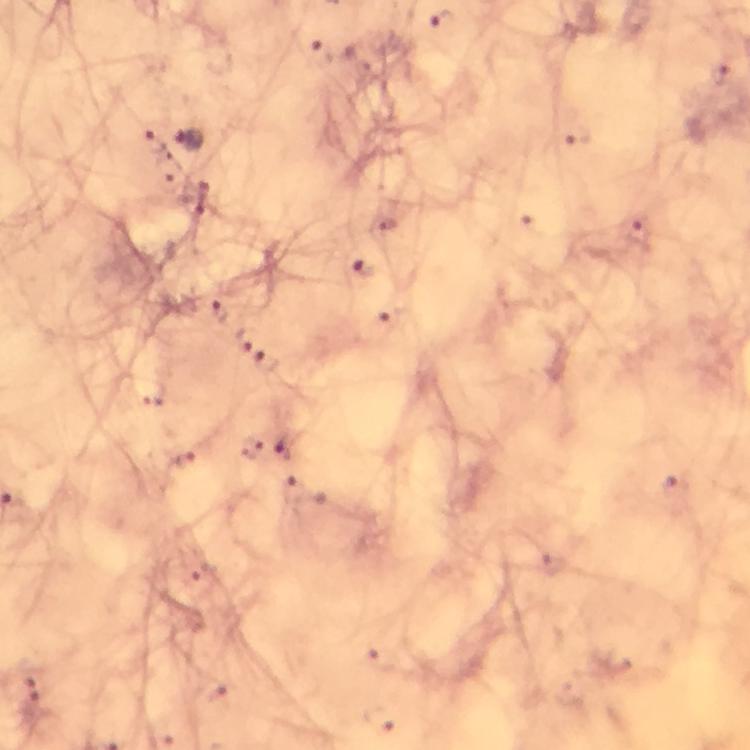
Approximate object centers, in pixels from the top-left corner. Malaria parasite locations: (x=445, y=20), (x=321, y=50), (x=580, y=135), (x=189, y=141), (x=153, y=144), (x=640, y=234), (x=365, y=270), (x=219, y=310), (x=386, y=322), (x=245, y=341), (x=267, y=363), (x=249, y=448), (x=287, y=449), (x=184, y=459), (x=674, y=483), (x=32, y=691), (x=218, y=694), (x=382, y=719). From a diagnostic examination for malaria. Image is 750×750 pixels. Cropped region of a single field of view. Smartphone photograph taken through a microscope. Giemsa stain. At 100x magnification. Immersion oil was used. Thick blood film.